Assess this cell for malaria.
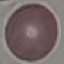
Uninfected.

stain = Giemsa
capture = smartphone camera at the microscope eyepiece
preparation = thin blood smear
image type = automatically extracted cell patch, resized to 64 × 64 pixels